Give the extent of all Trypanosoma brucei.
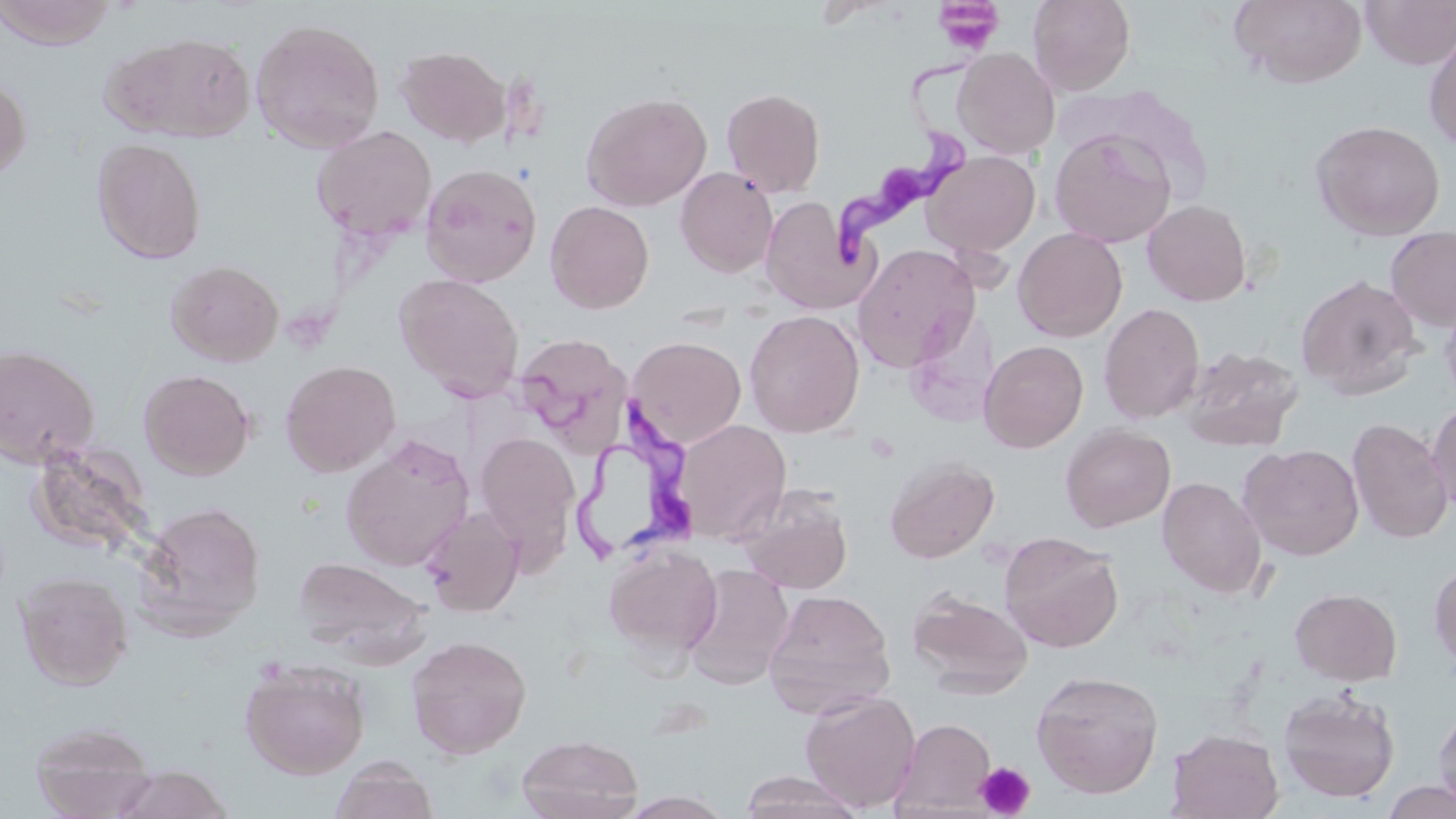

Approximate bounding boxes as (x1, y1, x2, y2) in pixels.
Trypanosoma brucei: (831, 59, 981, 269), (573, 408, 702, 565).

{
  "slide_level_diagnosis": "Trypanosoma brucei",
  "modality": "light microscopy",
  "platelet_locations": "approximate bounding boxes as (x1, y1, x2, y2) in pixels: (934, 1, 1003, 54), (975, 761, 1036, 818)",
  "stain": "May-Grünwald-Giemsa",
  "image_size": "1456×819 pixels",
  "magnification": "1000x",
  "field_of_view": "one of a larger specimen",
  "preparation": "thin blood film",
  "uninfected_red_blood_cell_locations": "approximate bounding boxes as (x1, y1, x2, y2) in pixels: (0, 0, 119, 49), (1027, 0, 1136, 96), (1229, 0, 1367, 87), (1360, 0, 1456, 70), (250, 16, 386, 153), (1423, 23, 1456, 152), (100, 30, 257, 143), (395, 44, 511, 147), (953, 47, 1060, 159), (0, 75, 31, 181), (1060, 85, 1213, 202), (721, 87, 826, 197), (581, 91, 712, 212), (1310, 119, 1446, 241), (311, 125, 437, 242), (1049, 127, 1178, 248), (92, 138, 207, 265), (922, 150, 1041, 259), (420, 162, 542, 287), (675, 166, 778, 278), (760, 196, 870, 314), (1142, 199, 1252, 306), (545, 200, 655, 314), (1013, 227, 1128, 342), (1385, 227, 1456, 332), (852, 243, 981, 372), (165, 259, 284, 366), (394, 273, 525, 401), (1296, 274, 1423, 399), (1440, 294, 1456, 409), (1098, 302, 1205, 424), (743, 310, 865, 438), (513, 333, 634, 454), (627, 335, 746, 448), (979, 340, 1089, 453), (0, 344, 101, 468), (1179, 345, 1304, 451), (280, 359, 401, 477), (139, 368, 255, 480), (1426, 400, 1456, 519), (1347, 417, 1454, 543), (674, 419, 792, 543), (1060, 424, 1175, 532), (475, 431, 580, 559), (340, 435, 475, 571), (27, 440, 155, 562), (1239, 443, 1364, 560), (884, 456, 1000, 564), (1157, 477, 1267, 597), (738, 485, 853, 594), (135, 500, 266, 640), (421, 507, 524, 617), (999, 531, 1124, 653), (604, 544, 722, 664), (292, 557, 429, 659), (1429, 560, 1456, 673), (683, 563, 794, 689), (16, 570, 134, 689), (907, 587, 1033, 699), (1289, 587, 1402, 686), (763, 588, 896, 719), (406, 635, 532, 759), (239, 658, 371, 779), (1030, 669, 1164, 799), (1277, 687, 1401, 803), (800, 690, 920, 812), (1432, 705, 1456, 813), (892, 718, 996, 816), (29, 719, 158, 818), (1166, 728, 1284, 818), (516, 733, 644, 819), (329, 759, 439, 819), (111, 765, 233, 819), (738, 771, 865, 819), (1381, 778, 1456, 819), (617, 791, 736, 819)"
}